Outline each blood parasite and name the species.
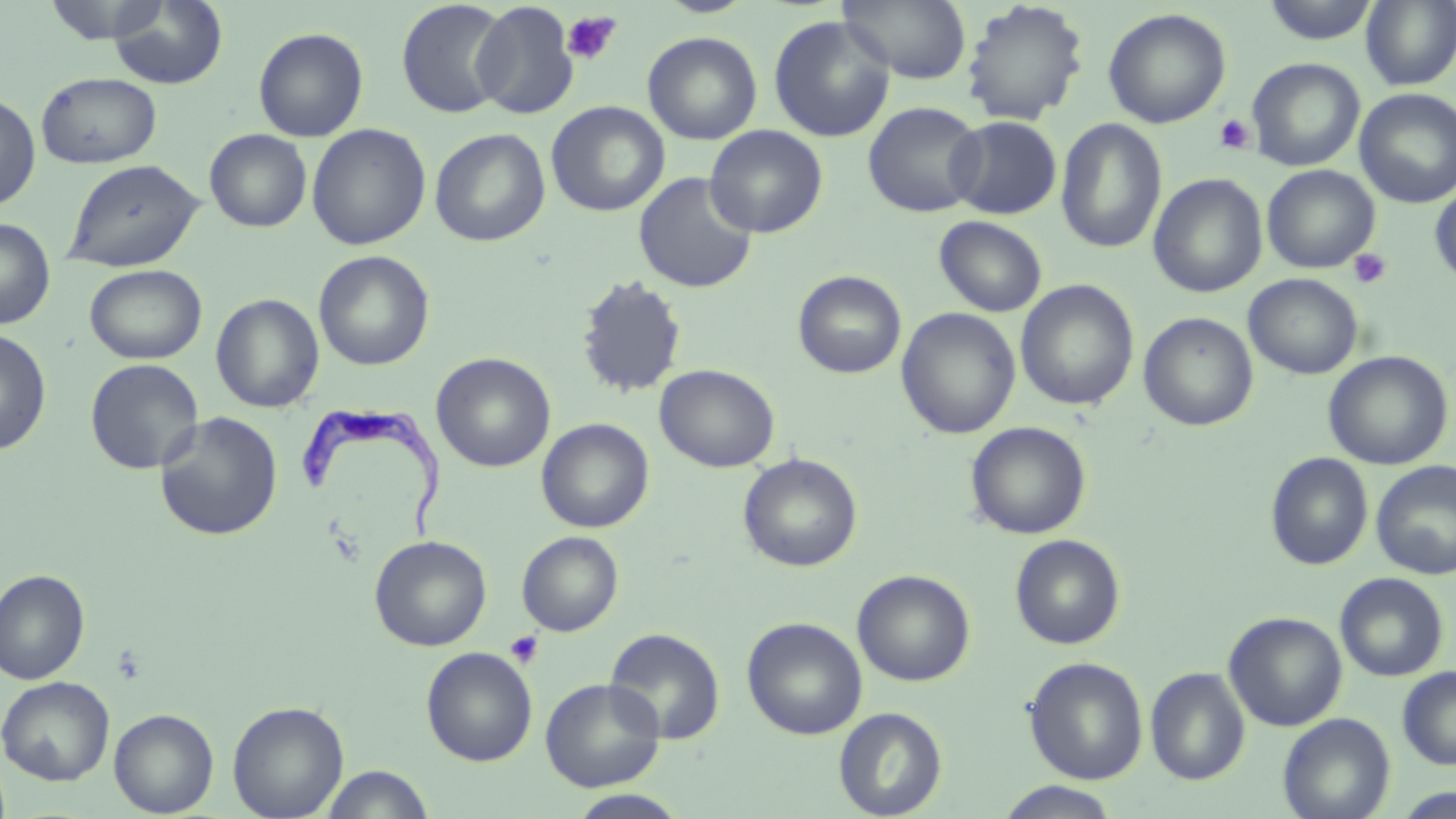
Approximate bounding boxes as (x1,y1)-(x2,y2) corner pairs in pixels.
Trypanosoma brucei: (292,399)-(450,542).
No Plasmodium falciparum, Plasmodium ovale, Plasmodium malariae, Plasmodium vivax, or Babesia divergens observed.

slide_level_diagnosis: Trypanosoma brucei
modality: optical microscopy
magnification: 1000x
platelet_locations: 'approximate bounding boxes as (x1,y1)-(x2,y2) corner pairs in pixels: (561,10)-(622,66), (1213,113)-(1255,154), (1348,248)-(1393,290), (504,630)-(545,669)'
field_of_view: one of a larger specimen
preparation: thin blood film
image_size: 1456×819 pixels
uninfected_red_blood_cell_locations: 'approximate bounding boxes as (x1,y1)-(x2,y2) corner pairs in pixels: (41,0)-(170,44), (837,0)-(971,84), (1260,0)-(1381,44), (109,1)-(228,89), (396,1)-(511,119), (471,1)-(579,119), (960,1)-(1090,126), (1360,1)-(1456,90), (1102,8)-(1232,129), (768,15)-(895,142), (253,26)-(369,142), (643,31)-(763,145), (1247,57)-(1365,172), (36,72)-(162,168), (1355,88)-(1456,208), (0,92)-(40,212), (863,100)-(986,217), (546,101)-(670,217), (947,116)-(1062,219), (1056,118)-(1167,254), (306,124)-(431,250), (705,125)-(828,238), (429,128)-(550,247), (205,129)-(312,232), (63,159)-(204,272), (1262,165)-(1380,273), (633,172)-(758,293), (1148,173)-(1268,298), (1430,181)-(1456,287), (934,216)-(1047,317), (0,217)-(55,329), (314,251)-(435,372), (84,264)-(207,364), (793,270)-(907,379), (576,274)-(687,398), (1244,274)-(1363,379), (1015,279)-(1140,411), (211,293)-(324,413), (897,307)-(1021,439), (1139,312)-(1258,431), (0,328)-(52,456), (1323,350)-(1453,470), (431,352)-(556,473), (85,358)-(204,474), (654,363)-(780,472), (154,412)-(283,541), (536,418)-(654,533), (966,421)-(1091,540), (1265,452)-(1373,571), (738,453)-(863,572), (1371,461)-(1456,580), (516,531)-(623,636), (1010,534)-(1125,650), (370,535)-(492,651), (0,569)-(90,685), (852,569)-(975,686), (1335,572)-(1449,682), (1224,611)-(1347,731), (742,616)-(868,740), (604,627)-(725,745), (421,646)-(538,766), (1024,656)-(1148,784), (1397,666)-(1456,770), (1145,667)-(1251,785), (0,675)-(115,786), (540,678)-(666,792), (227,699)-(349,818), (834,706)-(947,818), (109,708)-(218,817), (1278,712)-(1395,819), (319,764)-(436,818), (995,782)-(1123,819), (1392,787)-(1456,819), (567,789)-(691,818)'
stain: May-Grünwald-Giemsa